Comment on the morphology of the erythrocytes.
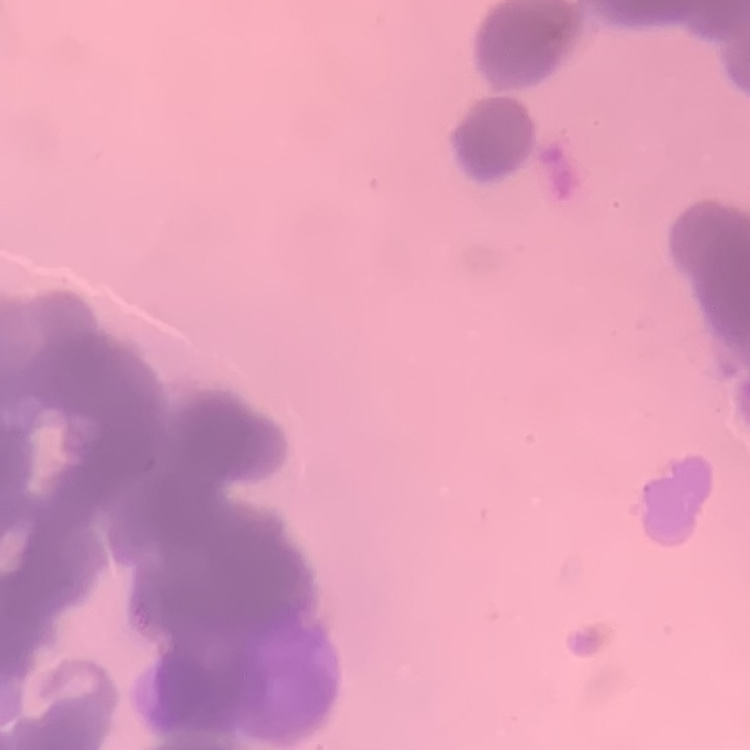
Rouleaux formation.

Thin blood film. One tile cut from a larger photomicrograph. Field's or Giemsa stain.